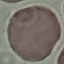

Summary:
  - Result: no malaria parasites detected
  - Image type: automatically extracted cell patch, resized to 64 × 64 pixels
  - Capture: smartphone through the microscope eyepiece
  - Preparation: thin blood film
  - Stain: Giemsa